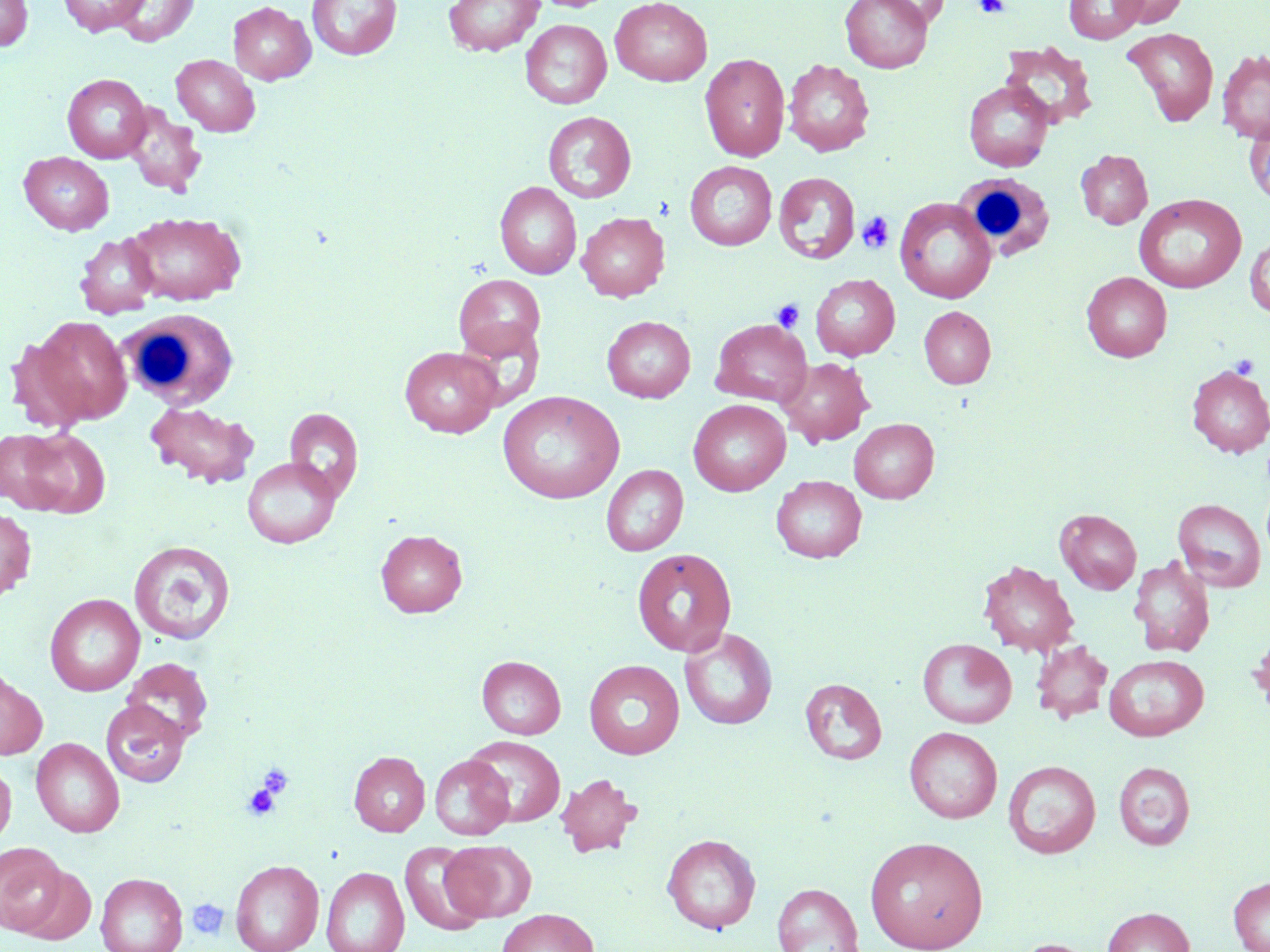

Approximate bounding boxes as named x1/y1/x2/y2 corners in pixels. White blood cell locations: (x1=956, y1=173, x2=1054, y2=259), (x1=118, y1=307, x2=239, y2=409). Uninfected red blood cell locations: (x1=0, y1=0, x2=33, y2=51), (x1=58, y1=0, x2=150, y2=36), (x1=111, y1=0, x2=198, y2=46), (x1=307, y1=0, x2=402, y2=61), (x1=443, y1=0, x2=544, y2=56), (x1=840, y1=0, x2=934, y2=73), (x1=1064, y1=0, x2=1147, y2=43), (x1=1112, y1=0, x2=1187, y2=27), (x1=228, y1=1, x2=315, y2=85), (x1=611, y1=1, x2=713, y2=86), (x1=520, y1=19, x2=612, y2=109), (x1=1123, y1=27, x2=1219, y2=126), (x1=1000, y1=41, x2=1098, y2=129), (x1=1217, y1=50, x2=1270, y2=143), (x1=700, y1=53, x2=790, y2=162), (x1=171, y1=54, x2=260, y2=136), (x1=783, y1=58, x2=875, y2=157), (x1=62, y1=74, x2=151, y2=163), (x1=963, y1=80, x2=1053, y2=172), (x1=121, y1=103, x2=207, y2=196), (x1=543, y1=111, x2=636, y2=203), (x1=1246, y1=117, x2=1270, y2=208), (x1=1076, y1=149, x2=1153, y2=229), (x1=19, y1=152, x2=114, y2=235), (x1=685, y1=161, x2=777, y2=250), (x1=773, y1=172, x2=860, y2=264), (x1=495, y1=181, x2=581, y2=279), (x1=1134, y1=194, x2=1246, y2=293), (x1=894, y1=197, x2=997, y2=304), (x1=125, y1=211, x2=246, y2=306), (x1=577, y1=212, x2=670, y2=301), (x1=74, y1=233, x2=161, y2=319), (x1=1245, y1=235, x2=1270, y2=317), (x1=1082, y1=272, x2=1172, y2=362), (x1=453, y1=274, x2=546, y2=360), (x1=810, y1=274, x2=900, y2=360), (x1=919, y1=306, x2=996, y2=389), (x1=31, y1=315, x2=132, y2=425), (x1=602, y1=315, x2=696, y2=403), (x1=454, y1=319, x2=546, y2=410), (x1=711, y1=319, x2=811, y2=405), (x1=400, y1=346, x2=502, y2=438), (x1=778, y1=357, x2=875, y2=447), (x1=1186, y1=365, x2=1270, y2=458), (x1=497, y1=391, x2=625, y2=503), (x1=144, y1=400, x2=259, y2=489), (x1=688, y1=400, x2=791, y2=496), (x1=284, y1=407, x2=364, y2=502), (x1=849, y1=418, x2=939, y2=503), (x1=12, y1=427, x2=110, y2=518), (x1=242, y1=456, x2=341, y2=548), (x1=600, y1=465, x2=688, y2=556), (x1=772, y1=475, x2=867, y2=563), (x1=1173, y1=498, x2=1266, y2=592), (x1=0, y1=508, x2=36, y2=601), (x1=1055, y1=508, x2=1141, y2=594), (x1=376, y1=528, x2=467, y2=618), (x1=129, y1=540, x2=236, y2=645), (x1=632, y1=548, x2=736, y2=656), (x1=1130, y1=555, x2=1215, y2=657), (x1=978, y1=560, x2=1079, y2=657), (x1=44, y1=593, x2=144, y2=696), (x1=679, y1=628, x2=778, y2=730), (x1=1250, y1=629, x2=1270, y2=720), (x1=917, y1=638, x2=1017, y2=728), (x1=1031, y1=640, x2=1113, y2=724), (x1=1104, y1=654, x2=1209, y2=741), (x1=477, y1=655, x2=566, y2=739), (x1=122, y1=657, x2=213, y2=747), (x1=584, y1=659, x2=685, y2=759), (x1=0, y1=666, x2=48, y2=760), (x1=800, y1=677, x2=887, y2=765), (x1=100, y1=700, x2=190, y2=787), (x1=904, y1=726, x2=1002, y2=823), (x1=467, y1=736, x2=565, y2=827), (x1=31, y1=737, x2=125, y2=838), (x1=349, y1=751, x2=430, y2=836), (x1=429, y1=755, x2=513, y2=840), (x1=1003, y1=760, x2=1101, y2=858), (x1=1113, y1=761, x2=1195, y2=850), (x1=0, y1=762, x2=16, y2=848), (x1=555, y1=773, x2=641, y2=857), (x1=661, y1=833, x2=761, y2=934), (x1=864, y1=836, x2=988, y2=951), (x1=0, y1=841, x2=67, y2=935), (x1=442, y1=841, x2=536, y2=922), (x1=401, y1=842, x2=489, y2=934), (x1=230, y1=859, x2=324, y2=952), (x1=14, y1=864, x2=96, y2=946), (x1=321, y1=866, x2=410, y2=952), (x1=96, y1=872, x2=188, y2=952), (x1=1228, y1=877, x2=1270, y2=952), (x1=772, y1=882, x2=864, y2=952), (x1=1102, y1=907, x2=1195, y2=952), (x1=497, y1=908, x2=599, y2=952), (x1=1010, y1=938, x2=1102, y2=952). Platelet locations: (x1=975, y1=0, x2=1009, y2=18), (x1=857, y1=212, x2=894, y2=253), (x1=771, y1=298, x2=805, y2=333), (x1=1230, y1=355, x2=1259, y2=379), (x1=257, y1=763, x2=294, y2=801), (x1=243, y1=782, x2=284, y2=821), (x1=187, y1=898, x2=229, y2=941). Slide-level diagnosis: no evidence of blood parasites. May-Grünwald-Giemsa-stained preparation. Captured at 1000x magnification. Light microscopy. One field of a larger specimen. Image is 1270×952 pixels. Thin blood smear.